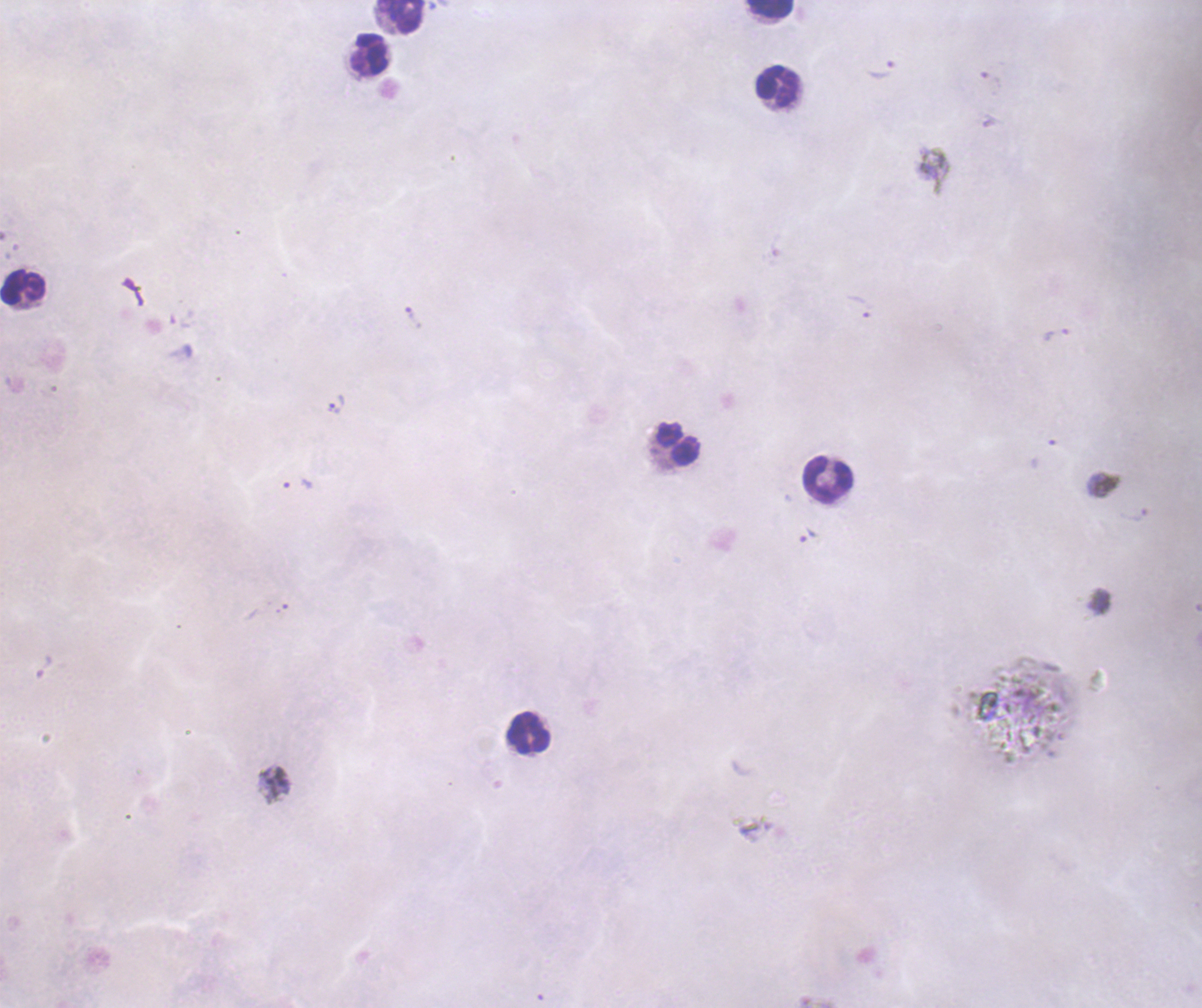
Approximate centers as {x, y} in pixels.
Summary:
  - Trophozoite locations: {881, 69}, {858, 306}, {413, 317}, {1055, 335}, {335, 405}, {297, 485}, {807, 536}
  - Leukocyte locations: {770, 9}, {401, 17}, {370, 54}, {777, 87}, {23, 288}, {679, 444}, {827, 479}, {529, 734}
  - Image size: 1202×1008 pixels
  - Context: previously used in a real diagnosis
  - Background quality: unsatisfactory
  - Field of view: single
  - Result: Plasmodium parasites detected
  - Coloration quality: bad
  - Stain: Romanowsky
  - Preparation: thick blood smear
  - Magnification: 100x